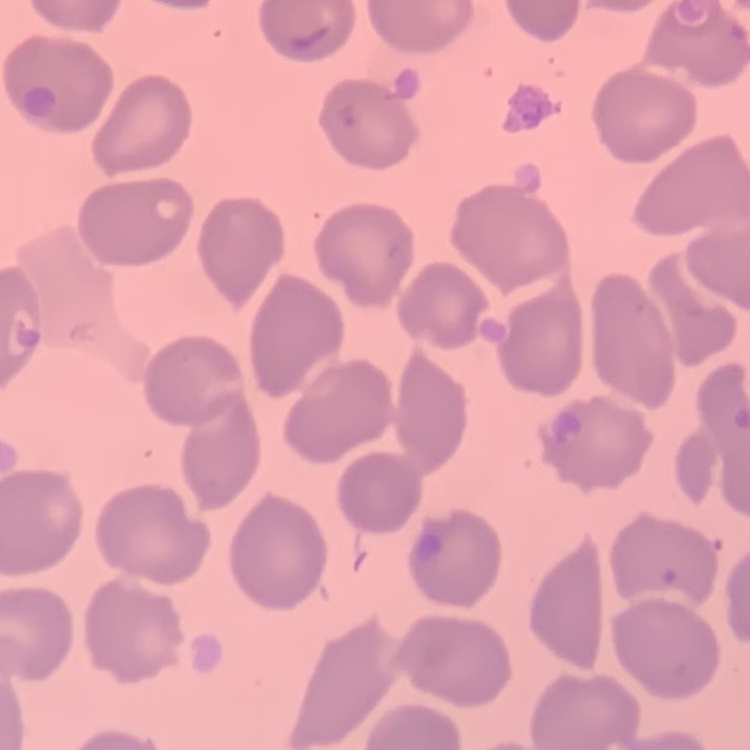

Summary:
  - Red blood cell morphology: no rouleaux formation
  - Stain: Field's or Giemsa
  - Preparation: thin blood film
  - Image type: square crop of a larger photomicrograph